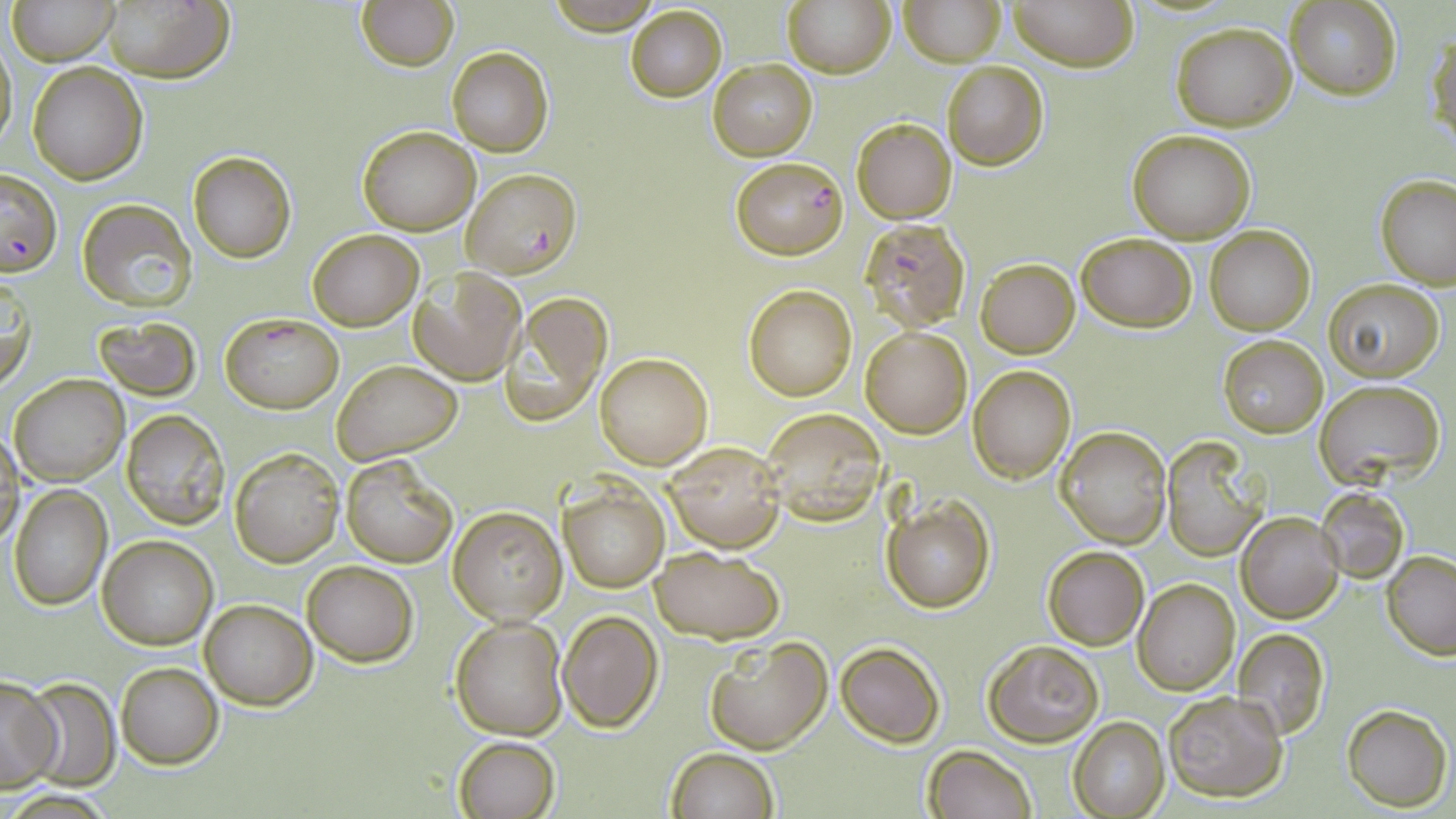

slide_level_diagnosis: Plasmodium falciparum
preparation: thin blood film
image_size: 1456×819 pixels
stain: May-Grünwald-Giemsa
plasmodium_falciparum_infected_red_blood_cell_locations: 'approximate bounding boxes as (x1,y1)-(x2,y2) corner pairs in pixels: (732,155)-(849,258), (1,166)-(63,276), (464,167)-(580,278), (858,217)-(973,332), (220,312)-(344,413)'
field_of_view: one of a larger specimen
uninfected_red_blood_cell_locations: 'approximate bounding boxes as (x1,y1)-(x2,y2) corner pairs in pixels: (7,0)-(120,66), (782,0)-(895,77), (899,0)-(1004,67), (1009,0)-(1136,72), (100,1)-(234,83), (357,1)-(459,72), (1283,1)-(1401,99), (541,3)-(668,33), (625,5)-(727,102), (1170,22)-(1297,131), (1429,27)-(1455,156), (0,35)-(16,155), (446,47)-(554,158), (708,59)-(818,161), (942,61)-(1048,169), (28,62)-(147,184), (851,117)-(957,224), (358,126)-(480,235), (1128,129)-(1257,244), (187,150)-(296,263), (1375,174)-(1456,289), (77,199)-(196,311), (1205,225)-(1316,335), (307,229)-(424,330), (1074,232)-(1197,332), (974,258)-(1079,358), (410,270)-(529,385), (1,272)-(35,391), (1322,279)-(1444,382), (744,284)-(856,401), (501,291)-(612,426), (94,316)-(203,401), (860,326)-(973,439), (1217,334)-(1328,438), (594,352)-(713,471), (332,359)-(462,465), (968,365)-(1076,483), (9,372)-(128,486), (1315,379)-(1444,489), (759,407)-(887,524), (120,410)-(230,529), (1056,426)-(1171,547), (0,431)-(23,551), (664,440)-(785,553), (1159,440)-(1270,562), (229,447)-(344,567), (341,454)-(459,567), (9,486)-(112,610), (559,486)-(668,592), (1316,487)-(1408,582), (882,497)-(995,614), (447,506)-(565,625), (1236,511)-(1343,623), (98,536)-(217,650), (1042,545)-(1149,651), (648,546)-(785,643), (1382,550)-(1456,658), (301,560)-(419,666), (1134,578)-(1240,695), (201,600)-(316,709), (558,610)-(662,731), (449,616)-(567,739), (1232,629)-(1329,741), (704,635)-(833,756), (983,640)-(1103,746), (835,641)-(945,747), (115,661)-(224,768), (0,676)-(62,792), (24,676)-(118,789), (1162,691)-(1288,803), (1342,705)-(1450,811), (1068,717)-(1170,819), (454,736)-(560,818), (666,746)-(778,819), (922,746)-(1036,819)'
modality: light microscopy
magnification: 1000x